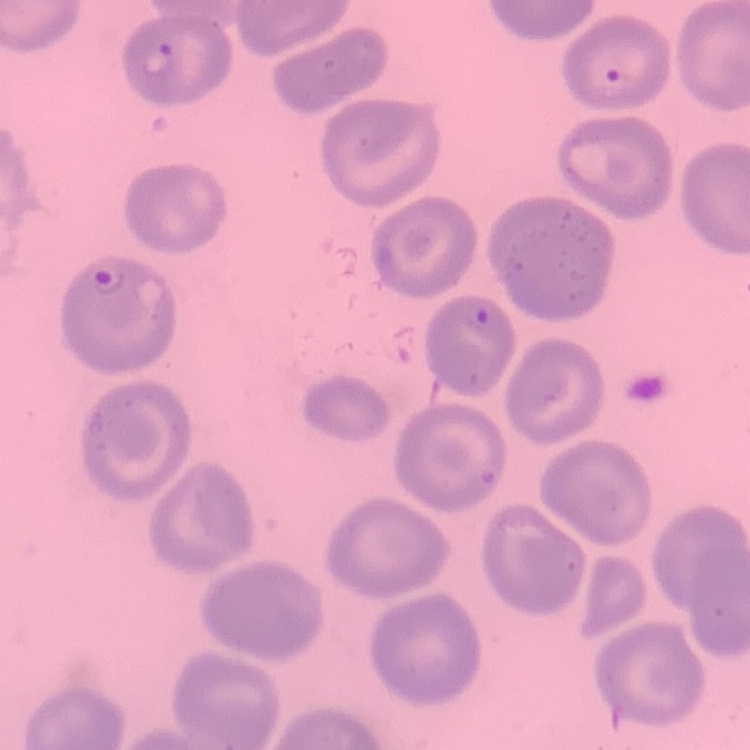

The red blood cells exhibit no rouleaux formation. Field's or Giemsa stain. Square crop of a larger photomicrograph. Thin peripheral smear.